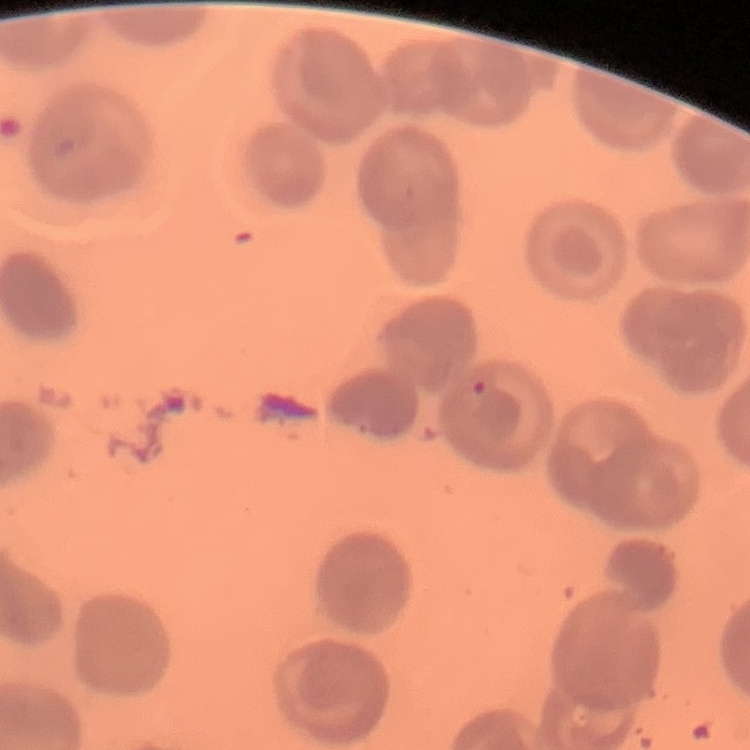

The red blood cells show no rouleaux formation. Thin blood film. Field's or Giemsa stain. One tile cut from a larger photomicrograph.